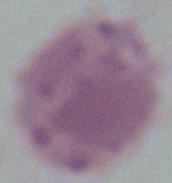
Summary:
  - Modality: micrograph
  - Magnification: 1000x
  - Identification: erythrocyte